State the blood parasite species.
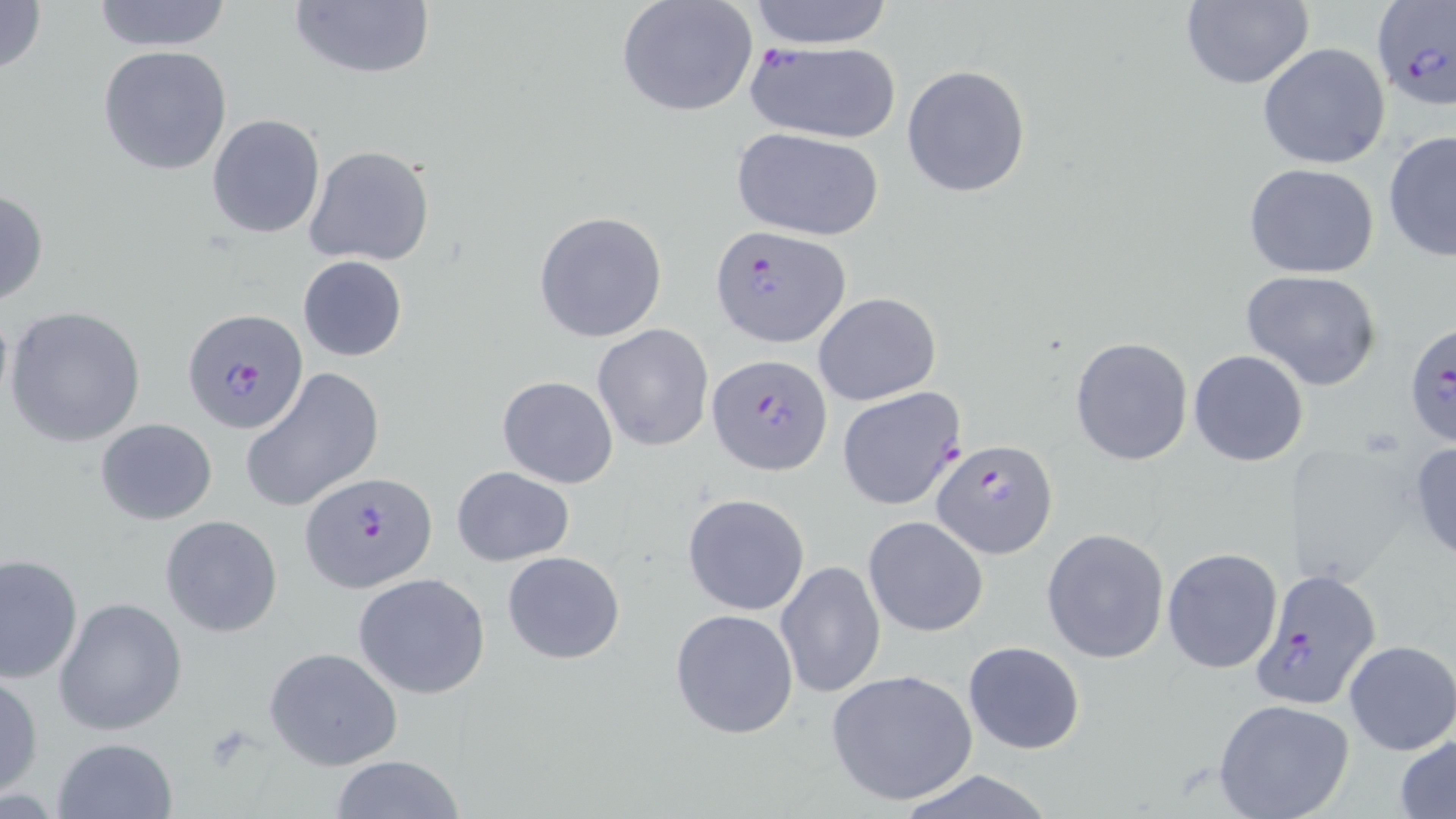

Plasmodium falciparum.

Summary:
  - Coordinate format: approximate bounding boxes as (x1, y1, x2, y2) in pixels
  - Uninfected red blood cell locations: (0, 0, 48, 81), (91, 0, 233, 52), (288, 0, 435, 82), (746, 0, 896, 49), (616, 1, 759, 119), (1178, 1, 1314, 90), (1258, 43, 1390, 170), (98, 44, 234, 177), (902, 64, 1032, 198), (206, 114, 325, 238), (732, 127, 884, 241), (1383, 129, 1456, 264), (303, 144, 436, 267), (1243, 164, 1382, 279), (0, 186, 49, 309), (534, 209, 668, 343), (298, 255, 408, 362), (1240, 270, 1384, 392), (813, 291, 941, 406), (5, 305, 147, 446), (592, 324, 714, 452), (1069, 336, 1194, 466), (1188, 349, 1309, 466), (242, 368, 385, 514), (496, 375, 618, 488), (95, 418, 217, 524), (1407, 440, 1456, 563), (1282, 442, 1420, 586), (452, 466, 574, 566), (682, 493, 810, 615), (160, 514, 283, 637), (865, 516, 988, 636), (1041, 527, 1169, 664), (1162, 548, 1283, 674), (503, 550, 624, 664), (0, 552, 84, 684), (775, 559, 886, 702), (353, 572, 492, 699), (52, 598, 189, 737), (669, 607, 799, 740), (962, 640, 1085, 754), (1344, 641, 1456, 754), (264, 646, 405, 770), (825, 669, 978, 808), (0, 672, 44, 799), (1212, 698, 1354, 819), (1395, 733, 1456, 818), (52, 737, 181, 819), (328, 755, 467, 819), (891, 769, 1060, 819)
  - Plasmodium falciparum-infected red blood cell locations: (1370, 2, 1455, 113), (745, 43, 905, 143), (711, 225, 851, 347), (185, 311, 311, 438), (1404, 319, 1456, 447), (710, 354, 832, 475), (836, 387, 966, 510), (932, 439, 1058, 559), (301, 471, 437, 592), (1249, 567, 1382, 710)
  - Field of view: one of a larger specimen
  - Image size: 1456×819 pixels
  - Magnification: 1000x
  - Stain: May-Grünwald-Giemsa
  - Modality: light microscopy
  - Preparation: thin blood smear